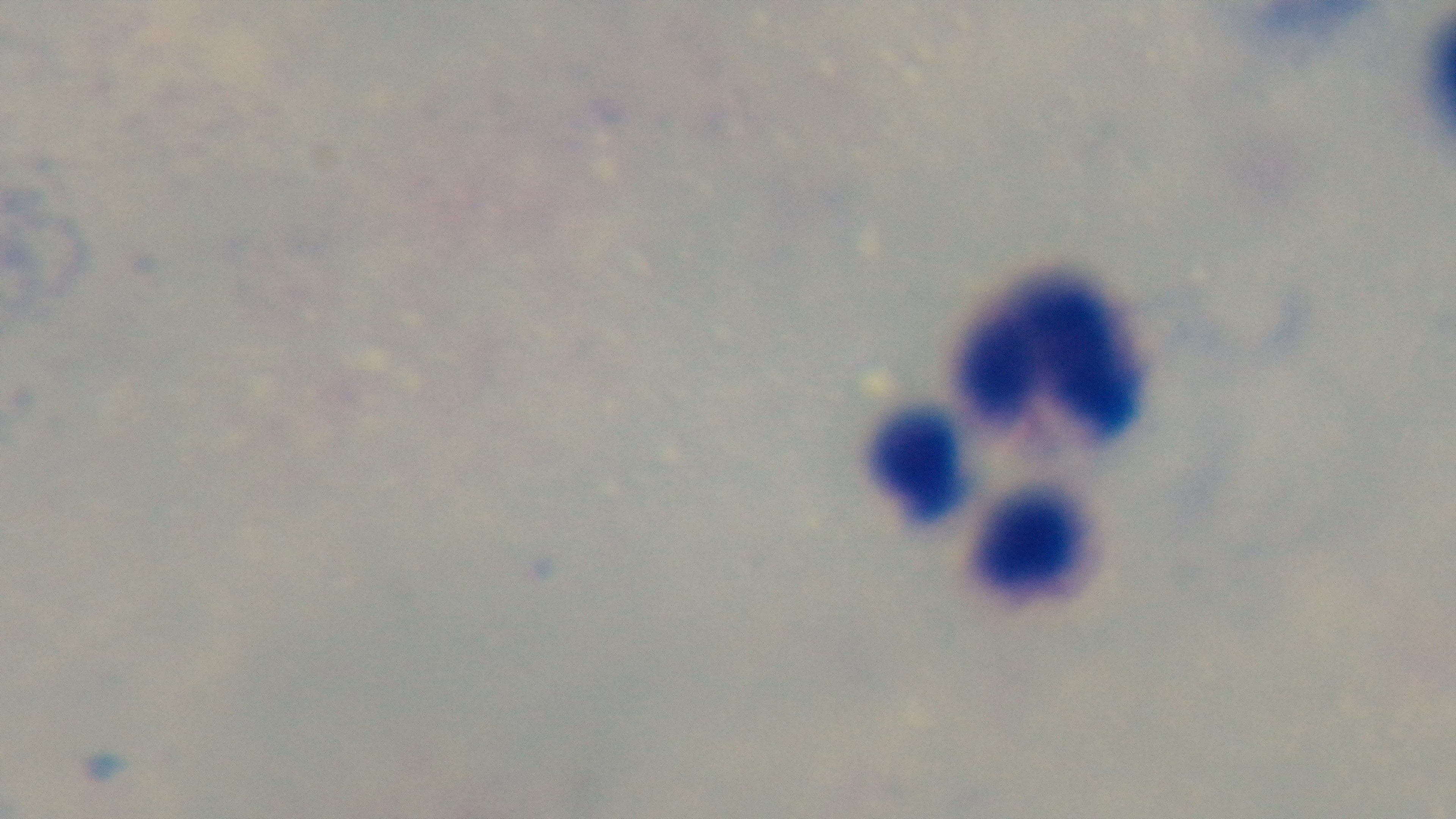

Summary:
  - Preparation: thick smear
  - Stain: Giemsa
  - Capture: mounted 4K digital camera
  - Objective: 100x oil immersion
  - Malaria status: uninfected
  - Field of view: one from the slide
  - Modality: light microscopy